Assess this cell for malaria.
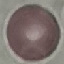

Uninfected.

preparation: thin blood smear
image_type: cell patch, automatically extracted from a larger field of view and resized to 64 × 64 pixels
stain: Giemsa
capture: smartphone camera at the microscope eyepiece